Locate every Plasmodium parasite.
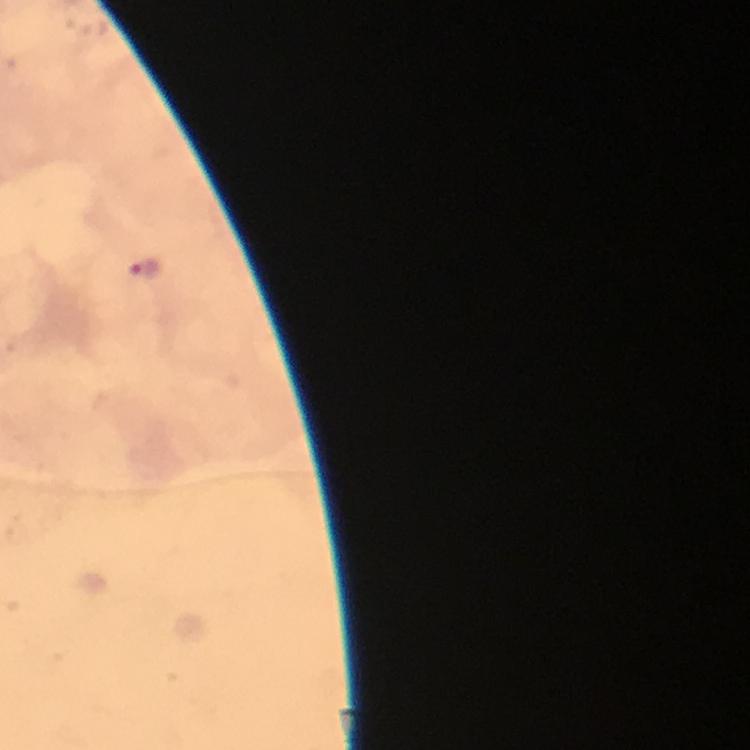
Approximate centers as {x, y} in pixels.
Plasmodium parasites: {143, 267}.

Summary:
  - Immersion oil: used
  - Image size: 750×750 pixels
  - Cropped from: a single field of view
  - Capture: smartphone mounted on the microscope
  - Preparation: thick blood smear
  - Context: from a diagnostic examination for malaria
  - Magnification: 100x
  - Stain: Giemsa